Give the extent of all Trypanosoma brucei.
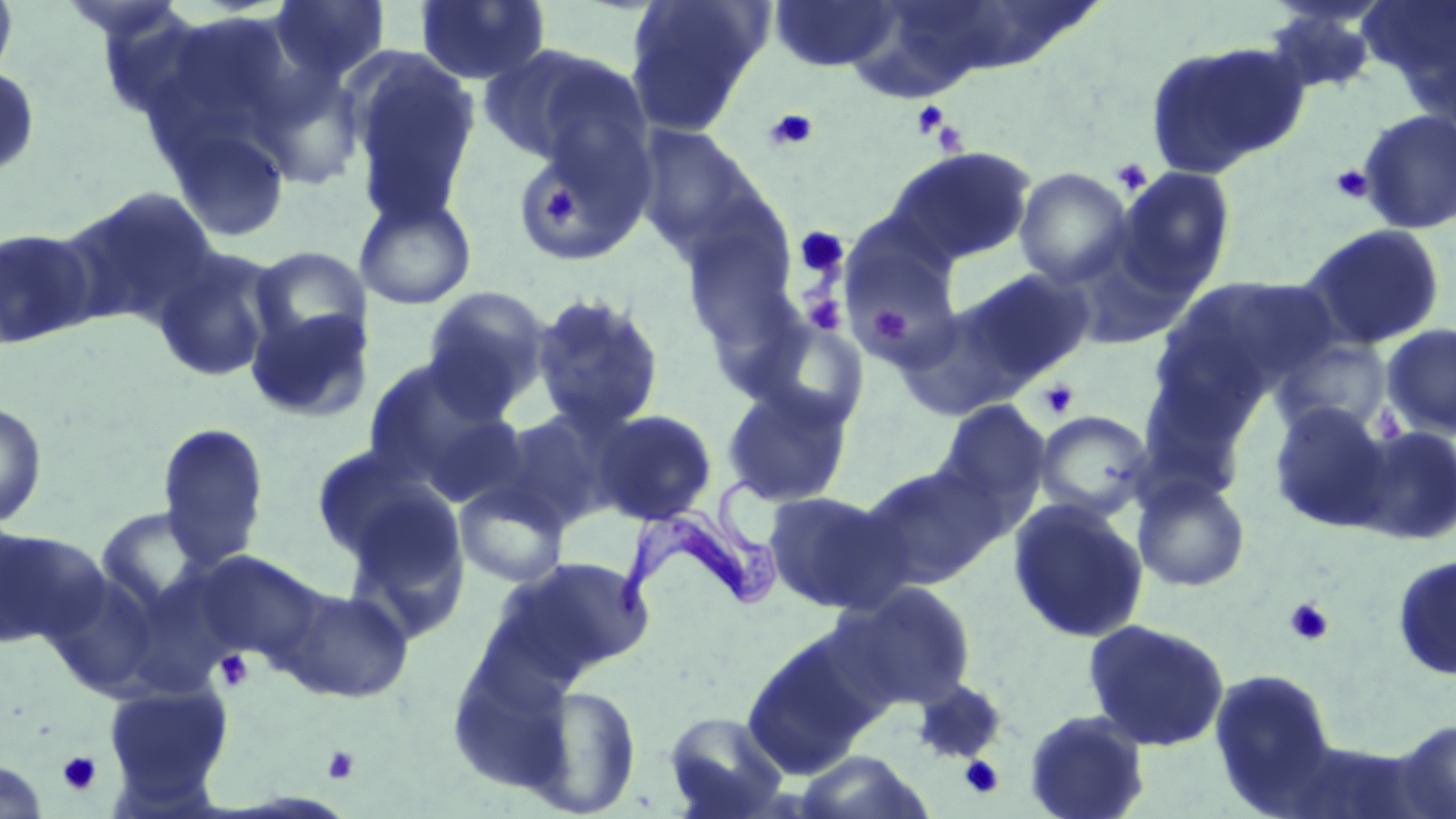
Approximate bounding boxes as [x1, y1, x2, y2] in pixels.
Trypanosoma brucei: [613, 478, 794, 621].

Uninfected red blood cell locations (subset): [0, 0, 18, 87], [269, 0, 390, 84], [414, 0, 551, 86], [624, 0, 770, 136], [768, 0, 901, 73], [1359, 0, 1456, 105], [1260, 5, 1384, 97], [1144, 40, 1309, 179], [476, 44, 624, 167], [346, 51, 481, 227], [0, 66, 41, 179], [1356, 109, 1456, 235], [165, 120, 293, 242], [633, 124, 764, 258], [510, 127, 650, 268], [885, 146, 1037, 266], [1013, 167, 1134, 288], [1113, 167, 1236, 295], [57, 186, 221, 331], [355, 192, 478, 310], [679, 210, 801, 348], [839, 222, 968, 365], [1299, 223, 1447, 352], [0, 226, 100, 349], [1062, 236, 1194, 350], [151, 245, 284, 383], [250, 246, 371, 355], [964, 267, 1096, 382], [1159, 275, 1334, 406], [421, 286, 554, 417], [530, 292, 666, 436], [895, 302, 1024, 421], [245, 304, 373, 424], [740, 313, 870, 432], [1380, 324, 1456, 439], [1271, 337, 1394, 438], [362, 356, 512, 488], [720, 384, 855, 507], [934, 400, 1051, 517], [0, 401, 48, 528], [1267, 401, 1394, 532], [590, 409, 718, 525], [492, 410, 615, 532], [1033, 410, 1155, 522], [155, 422, 270, 572], [1350, 424, 1456, 545], [310, 446, 442, 563], [859, 462, 1008, 590], [1132, 473, 1251, 592], [454, 479, 571, 588], [340, 486, 470, 635], [763, 490, 906, 613], [1007, 499, 1149, 643], [94, 505, 215, 614], [0, 524, 85, 647], [197, 550, 328, 670], [1391, 553, 1456, 682], [506, 555, 655, 678], [42, 570, 163, 700], [834, 582, 978, 712], [278, 586, 414, 703], [1082, 618, 1230, 752], [742, 633, 875, 779], [1208, 667, 1340, 814], [103, 683, 233, 799], [527, 684, 643, 817], [663, 710, 790, 819], [1022, 710, 1150, 819], [1394, 718, 1456, 819], [1279, 739, 1436, 819], [793, 751, 935, 818], [0, 758, 48, 819]. Platelet locations (subset): [911, 99, 950, 139], [763, 108, 819, 152], [916, 109, 960, 151], [1111, 157, 1153, 195], [1331, 164, 1375, 203], [534, 182, 580, 231], [793, 226, 849, 280], [804, 295, 846, 335], [870, 306, 911, 345], [1036, 378, 1080, 420], [1370, 405, 1408, 447], [1284, 598, 1335, 646], [215, 649, 255, 692], [322, 745, 361, 786], [57, 750, 102, 795], [960, 756, 1004, 798]. Slide-level diagnosis: Trypanosoma brucei. Light microscopy. Image is 1456×819 pixels. May-Grünwald-Giemsa stain. Thin blood film. Single field of view. 1000x magnification.